Identify the parasite.
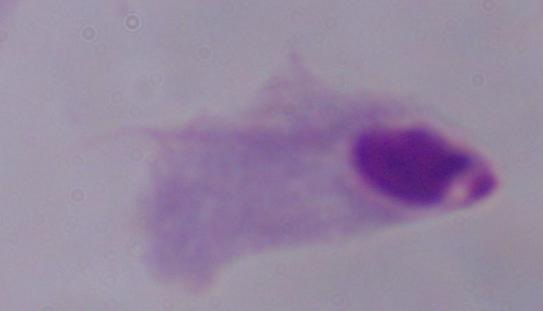

A trichomonad.

Summary:
  - Magnification: 1000x
  - Modality: photomicrograph